Name the blood parasite species.
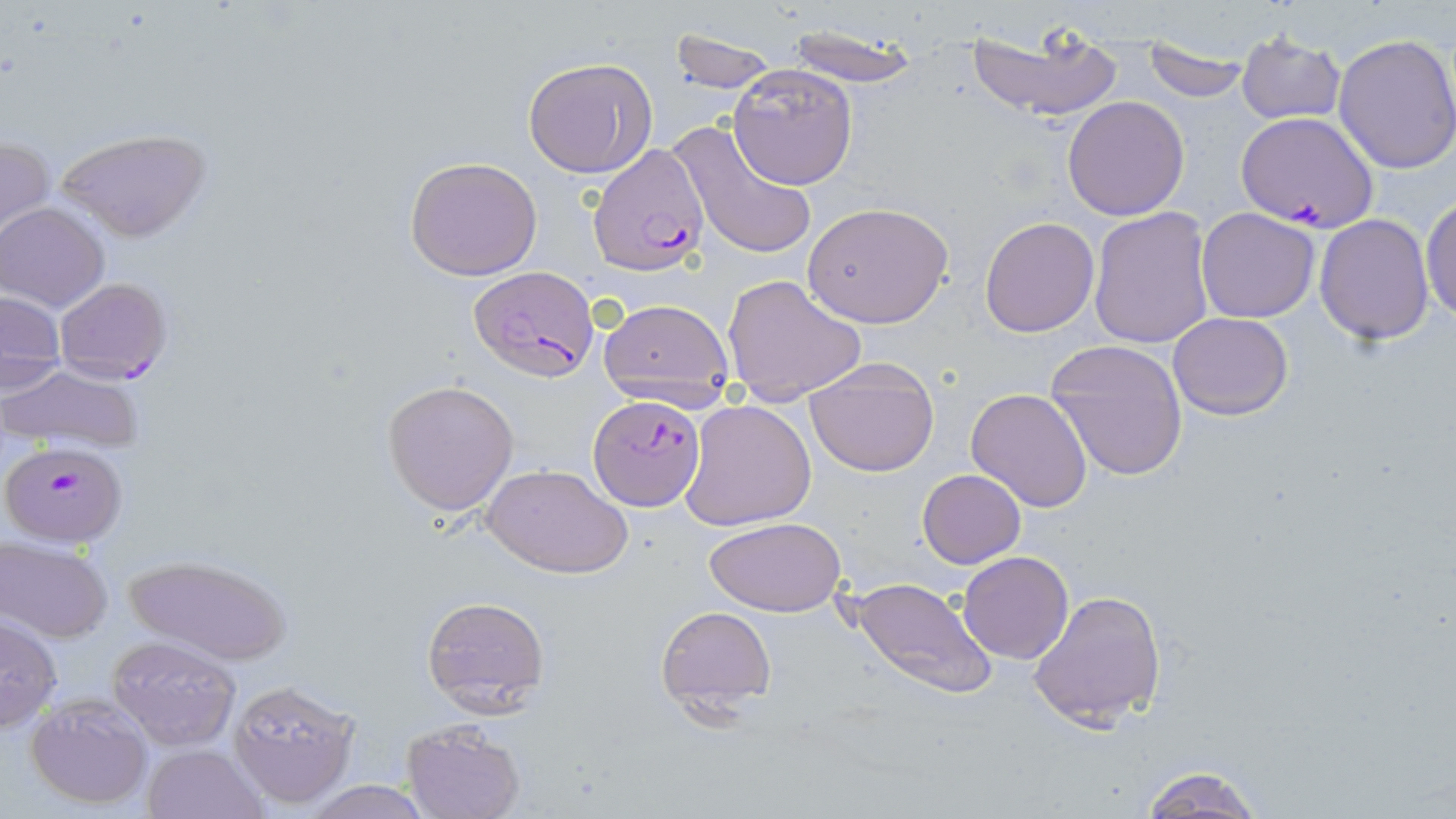

Plasmodium falciparum.

{
  "preparation": "thin blood film",
  "plasmodium_falciparum_infected_red_blood_cell_locations": "approximate bounding boxes as (x1, y1, x2, y2) in pixels: (1234, 110, 1377, 233), (588, 145, 709, 276), (469, 266, 597, 383), (54, 278, 172, 385), (589, 398, 706, 510), (5, 443, 127, 547)",
  "magnification": "1000x",
  "stain": "May-Grünwald-Giemsa",
  "modality": "optical microscopy",
  "image_size": "1456×819 pixels",
  "uninfected_red_blood_cell_locations": "approximate bounding boxes as (x1, y1, x2, y2) in pixels: (967, 19, 1126, 124), (786, 24, 917, 86), (669, 28, 779, 94), (1141, 30, 1249, 103), (1235, 33, 1346, 125), (1332, 34, 1456, 176), (524, 57, 658, 179), (727, 63, 858, 189), (1062, 96, 1190, 221), (671, 121, 817, 262), (56, 128, 210, 243), (1, 135, 53, 245), (405, 156, 545, 282), (1420, 193, 1455, 325), (804, 199, 954, 329), (1, 203, 110, 312), (1196, 207, 1320, 322), (1088, 208, 1214, 348), (1315, 213, 1436, 344), (979, 217, 1101, 337), (721, 273, 868, 400), (1, 290, 65, 381), (596, 295, 735, 396), (1168, 312, 1293, 420), (1046, 338, 1189, 482), (804, 357, 944, 477), (1, 364, 144, 451), (382, 380, 519, 514), (966, 388, 1094, 514), (679, 400, 816, 531), (481, 461, 631, 578), (916, 469, 1024, 569), (704, 517, 845, 618), (1, 538, 112, 642), (957, 551, 1073, 663), (121, 552, 290, 666), (848, 575, 998, 703), (1027, 588, 1168, 730), (419, 594, 550, 718), (656, 605, 777, 714), (0, 615, 62, 733), (108, 634, 242, 749), (227, 678, 360, 809), (25, 693, 154, 811), (401, 722, 525, 819), (140, 744, 269, 819), (1140, 765, 1263, 819), (295, 780, 437, 818)",
  "field_of_view": "single"
}